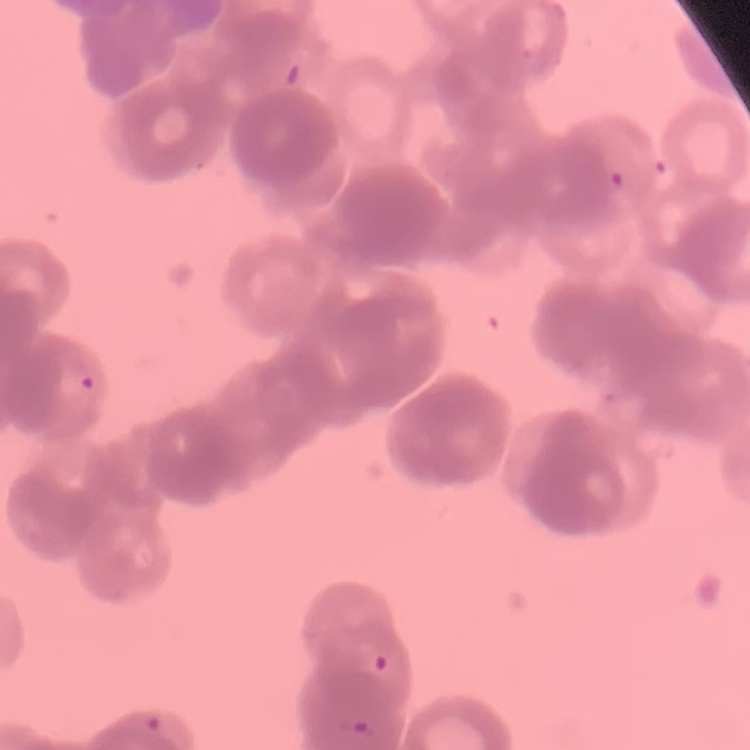 The erythrocytes show rouleaux formation. Field's or Giemsa stain. Thin peripheral smear. Square crop of a larger photomicrograph.